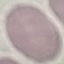
malaria status = uninfected
stain = Giemsa
preparation = thin blood smear
image type = cell patch, automatically extracted from a larger field of view and resized to 64 × 64 pixels
capture = smartphone camera at the microscope eyepiece